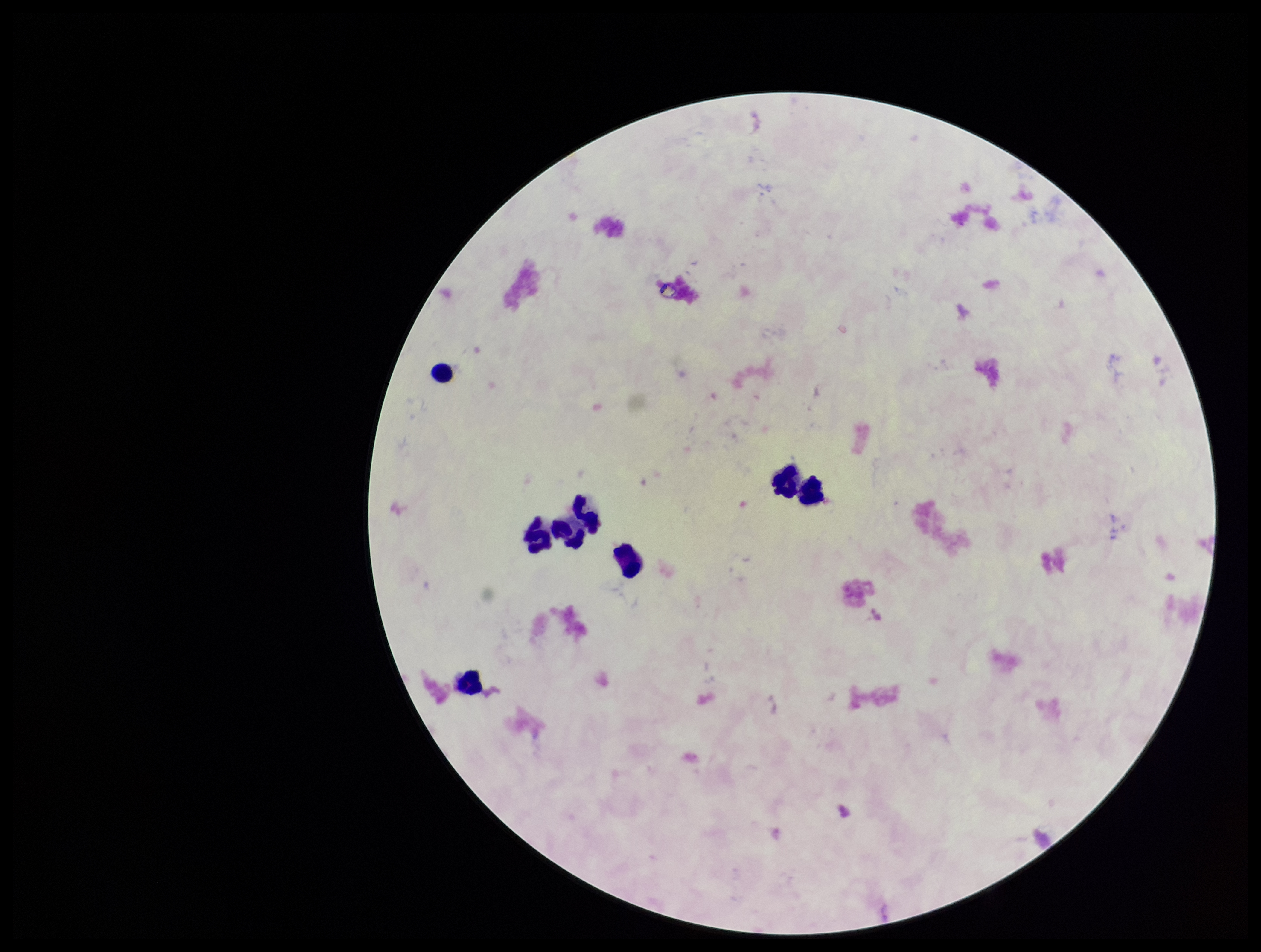
Plasmodium parasites: none seen. Image is 1261×952 pixels. Stained with Giemsa. Leukocyte count: 8. Photographed through the microscope eyepiece with a smartphone camera. Parasite count: 0. Single field of view. Preparation: thick. Patient malaria status: negative.